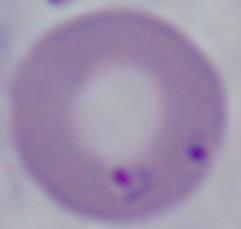
{
  "identification": "Babesia",
  "modality": "photomicrograph",
  "magnification": "1000x"
}